Locate every Plasmodium ovale-infected red blood cell.
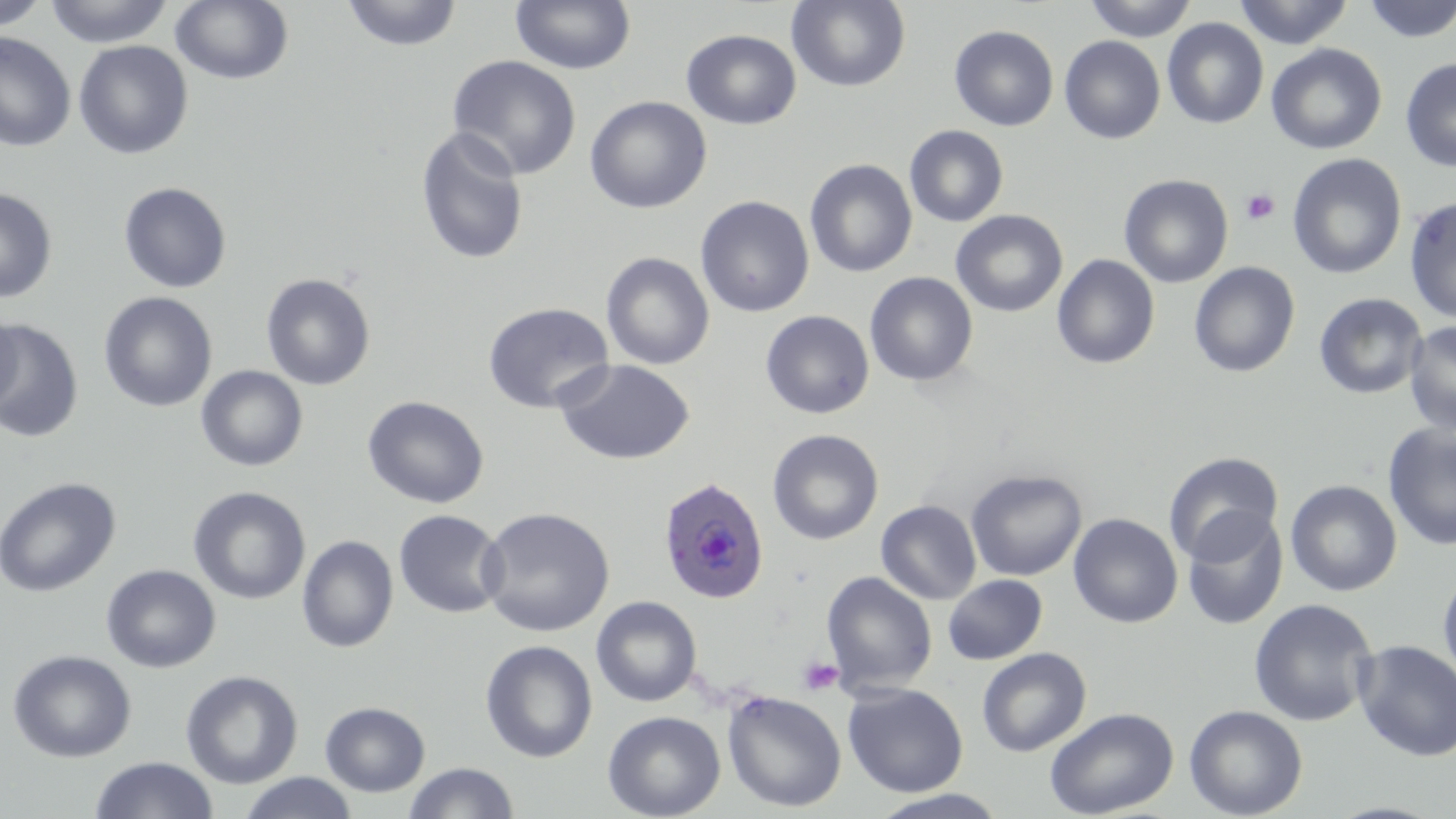
Approximate bounding boxes as (x1, y1, x2, y2) in pixels.
Plasmodium ovale-infected red blood cells: (658, 476, 769, 605).

slide_level_diagnosis: Plasmodium ovale
uninfected_red_blood_cell_locations: 'approximate bounding boxes as (x1, y1, x2, y2) in pixels: (0, 0, 50, 31), (44, 0, 174, 47), (170, 0, 294, 86), (341, 0, 462, 52), (510, 0, 635, 74), (786, 0, 911, 92), (1084, 0, 1198, 41), (1233, 0, 1354, 48), (1361, 0, 1456, 43), (1162, 17, 1268, 129), (949, 25, 1059, 131), (681, 29, 801, 130), (0, 31, 76, 152), (1060, 36, 1166, 144), (73, 40, 193, 159), (1266, 43, 1387, 154), (446, 54, 582, 179), (1400, 57, 1456, 173), (585, 96, 712, 214), (904, 125, 1009, 227), (414, 126, 530, 266), (1287, 153, 1407, 279), (804, 159, 917, 278), (1119, 174, 1233, 288), (118, 182, 233, 293), (0, 188, 58, 303), (1404, 195, 1456, 324), (696, 196, 814, 317), (951, 210, 1067, 317), (601, 252, 715, 370), (1052, 254, 1160, 370), (1188, 261, 1300, 377), (864, 272, 978, 386), (261, 273, 376, 390), (98, 291, 218, 412), (1314, 293, 1428, 399), (482, 302, 614, 414), (0, 310, 22, 414), (760, 310, 874, 419), (1, 320, 84, 443), (1404, 320, 1456, 437), (554, 358, 695, 466), (195, 365, 308, 472), (362, 395, 489, 509), (1382, 423, 1456, 551), (767, 429, 884, 545), (1165, 453, 1285, 566), (965, 469, 1087, 581), (0, 477, 121, 598), (1285, 479, 1402, 596), (1279, 482, 1394, 730), (188, 486, 311, 605), (876, 500, 982, 604), (478, 506, 615, 637), (393, 509, 507, 618), (1182, 510, 1288, 630), (1068, 513, 1183, 628), (296, 535, 399, 653), (101, 564, 221, 673), (1438, 569, 1456, 689), (822, 571, 937, 694), (942, 574, 1047, 665), (591, 596, 702, 707), (1248, 598, 1378, 727), (1353, 639, 1456, 762), (480, 640, 598, 763), (977, 647, 1091, 757), (7, 649, 137, 762), (181, 670, 303, 789), (843, 682, 968, 797), (722, 690, 847, 812), (320, 701, 430, 797), (1184, 704, 1308, 819), (1044, 706, 1179, 818), (602, 710, 726, 819), (88, 756, 218, 819), (403, 762, 520, 819), (238, 772, 359, 819), (868, 789, 1010, 818)'
modality: optical microscopy
magnification: 1000x
field_of_view: single
stain: May-Grünwald-Giemsa
platelet_locations: 'approximate bounding boxes as (x1, y1, x2, y2) in pixels: (1241, 188, 1281, 225), (797, 656, 844, 696)'
image_size: 1456×819 pixels
preparation: thin blood smear